Give the position of every malaria parasite.
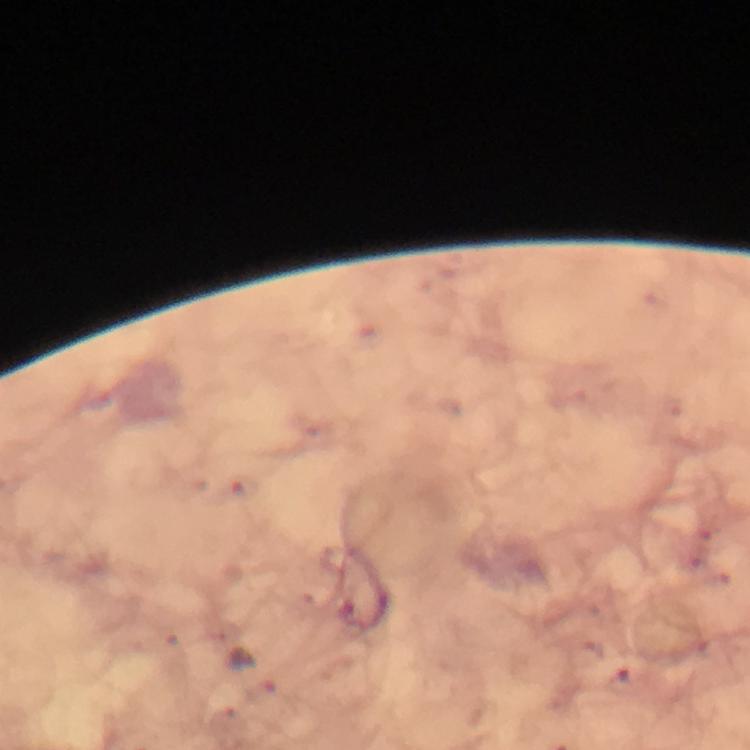

Approximate centers as {x, y} in pixels.
Malaria parasites: {254, 674}, {622, 680}.

Image is 750×750 pixels. At 100x magnification. Immersion oil was used. Photographed through the microscope with a smartphone camera. A crop from one field of view. Giemsa-stained preparation. Thick blood smear. From a malaria diagnostic workup.